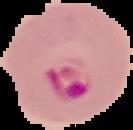
preparation: thin blood smear
malaria_status: parasitized
image_size: 133×130 pixels
image_type: cell region segmented out of the field of view; surrounding area masked to black